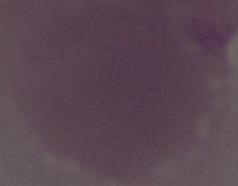
An erythrocyte is shown. Captured at 1000x magnification. Photomicrograph.